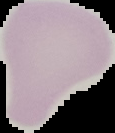
Summary:
  - Image size: 115×133 pixels
  - Result: no malaria parasites seen
  - Preparation: thin blood film
  - Image type: cell region segmented out of the field of view; surrounding area masked to black